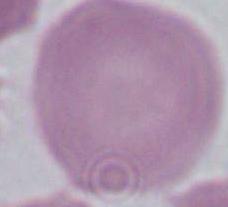 Captured at 1000x magnification. A red blood cell is shown. Micrograph.